Classify this cell by malaria status.
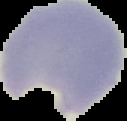
It is parasitized.

Summary:
  - Image size: 127×121 pixels
  - Preparation: thin blood film
  - Image type: segmented cell region on a black background